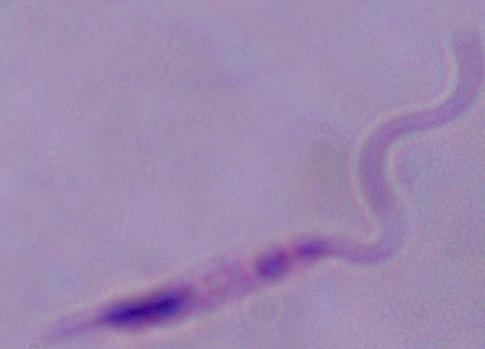
Summary:
  - Identification: Leishmania
  - Modality: micrograph
  - Magnification: 1000x